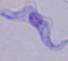
Summary:
  - Modality: photomicrograph
  - Magnification: 1000x
  - Identification: trypanosome